Outline each blood parasite and name the species.
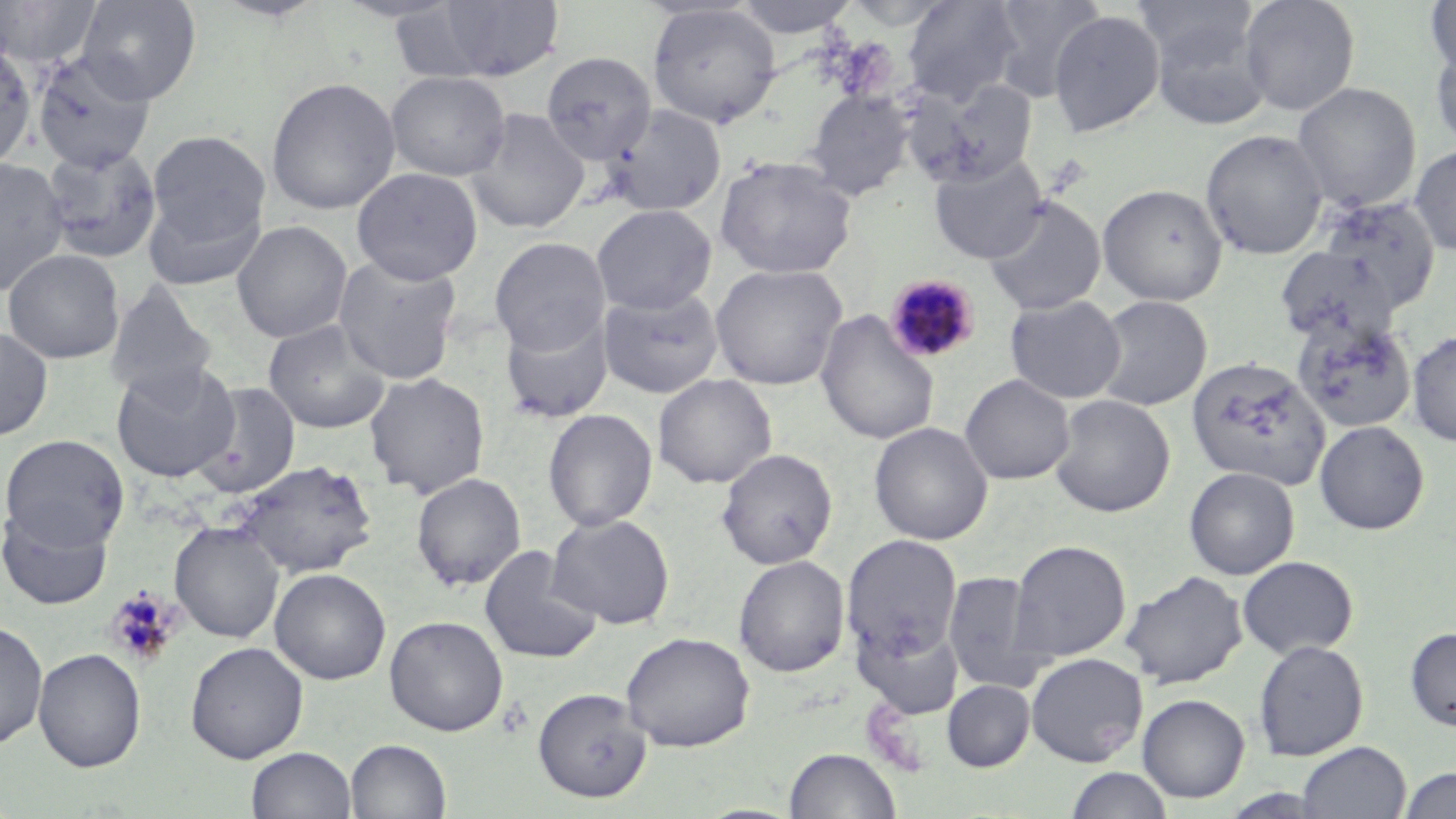
Approximate bounding boxes as (x1, y1, x2, y2) in pixels.
Plasmodium malariae-infected red blood cells: (884, 273, 983, 365).
No Plasmodium falciparum, Plasmodium ovale, Plasmodium vivax, Babesia divergens, or Trypanosoma brucei observed.

Uninfected red blood cell locations: (1, 0, 102, 70), (76, 0, 202, 105), (211, 0, 329, 22), (330, 0, 468, 23), (731, 0, 861, 38), (902, 0, 1024, 106), (987, 0, 1106, 102), (1239, 0, 1360, 116), (1424, 0, 1455, 81), (431, 1, 565, 81), (1133, 1, 1259, 70), (647, 5, 782, 129), (1047, 9, 1164, 138), (1147, 11, 1273, 130), (1429, 38, 1456, 153), (0, 43, 36, 171), (31, 51, 157, 171), (541, 51, 656, 166), (386, 71, 511, 181), (265, 77, 401, 215), (907, 78, 1038, 187), (1293, 82, 1422, 212), (804, 89, 915, 200), (607, 103, 727, 216), (466, 108, 590, 233), (1201, 129, 1328, 259), (146, 130, 270, 248), (41, 143, 163, 264), (1410, 143, 1456, 256), (928, 154, 1048, 264), (715, 155, 857, 279), (0, 156, 70, 295), (351, 168, 483, 285), (1098, 183, 1228, 306), (143, 188, 268, 291), (983, 195, 1106, 316), (1312, 195, 1443, 315), (592, 204, 716, 315), (231, 220, 353, 343), (489, 236, 610, 355), (1275, 246, 1400, 345), (3, 249, 125, 364), (333, 254, 462, 384), (710, 263, 847, 390), (104, 282, 217, 401), (599, 287, 724, 399), (1004, 295, 1126, 404), (1091, 295, 1212, 412), (500, 309, 614, 425), (815, 309, 940, 445), (1291, 316, 1418, 433), (262, 319, 391, 434), (0, 325, 54, 441), (1407, 330, 1456, 446), (1186, 355, 1330, 491), (112, 360, 238, 483), (364, 371, 491, 499), (960, 373, 1074, 484), (653, 374, 776, 489), (191, 380, 302, 498), (1049, 394, 1176, 517), (543, 408, 658, 532), (1314, 420, 1430, 535), (869, 421, 993, 545), (1, 434, 129, 551), (716, 448, 837, 569), (233, 459, 378, 579), (1183, 466, 1300, 580), (411, 472, 526, 591), (0, 506, 115, 611), (547, 513, 675, 629), (170, 521, 285, 643), (842, 534, 963, 662), (1009, 540, 1131, 663), (478, 545, 603, 665), (733, 555, 849, 677), (1237, 555, 1359, 659), (269, 568, 391, 685), (1120, 570, 1248, 689), (943, 571, 1048, 691), (384, 615, 508, 736), (0, 619, 48, 749), (854, 621, 963, 720), (1404, 627, 1456, 731), (620, 631, 756, 752), (1253, 639, 1369, 761), (185, 641, 309, 764), (33, 648, 146, 773), (1026, 652, 1148, 766), (942, 679, 1035, 771), (533, 687, 651, 803), (1137, 693, 1250, 803), (345, 739, 451, 819), (1297, 741, 1410, 819), (247, 746, 356, 819), (784, 747, 901, 818), (1064, 767, 1174, 819), (1400, 767, 1456, 818). Platelet locations: (105, 587, 179, 666). Slide-level diagnosis: Plasmodium malariae. 1000x magnification. Thin blood smear. Optical microscopy. Image is 1456×819 pixels. May-Grünwald-Giemsa-stained preparation. Single field of view.